Report the malaria status of this cell.
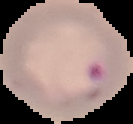
Parasitized.

From a thin blood smear. Segmented cell region on a black background. Image is 133×124 pixels.